Report the malaria status of this cell.
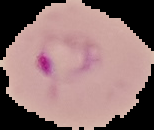
It is parasitized.

Summary:
  - Preparation: thin blood smear
  - Image type: segmented cell region on a black background
  - Image size: 154×130 pixels